Locate every blood parasite and identify its species.
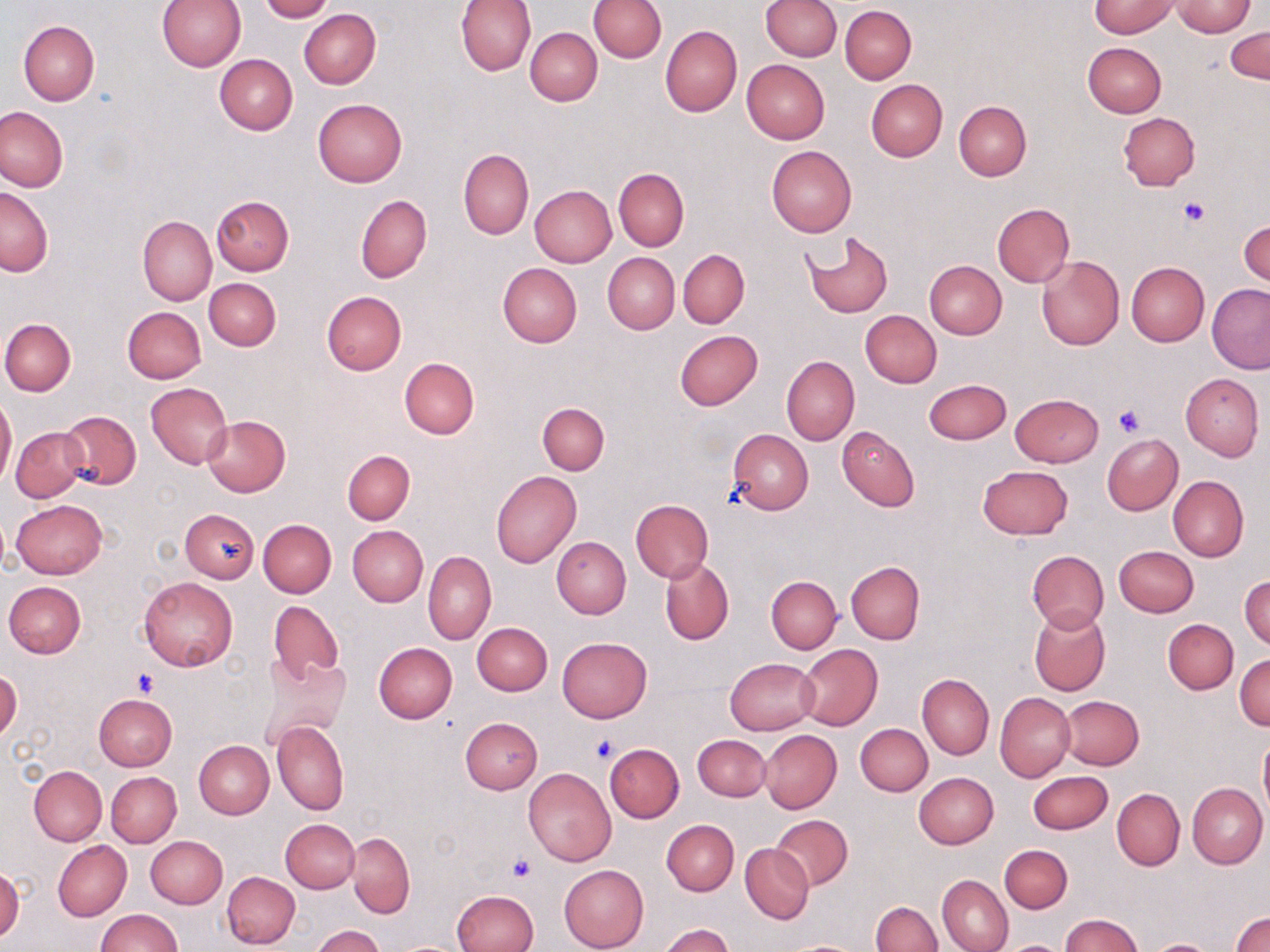
No blood parasites observed.

slide-level diagnosis = negative for blood parasites
uninfected red blood cell locations = approximate bounding boxes as (x1,y1)-(x2,y2) corner pairs in pixels: (259,0)-(332,22), (456,0)-(536,76), (589,0)-(666,63), (761,0)-(841,61), (157,1)-(245,72), (1089,2)-(1180,39), (1171,2)-(1257,37), (840,5)-(917,83), (299,8)-(381,89), (18,20)-(99,104), (660,24)-(742,117), (525,27)-(602,105), (1227,27)-(1270,84), (1083,42)-(1167,117), (215,53)-(297,134), (741,59)-(830,143), (866,80)-(947,161), (312,98)-(407,188), (954,100)-(1031,181), (0,106)-(70,193), (1118,113)-(1200,191), (766,145)-(857,236), (458,149)-(534,239), (614,169)-(689,251), (530,185)-(616,267), (0,187)-(54,276), (211,194)-(294,275), (355,195)-(432,283), (992,203)-(1074,286), (138,215)-(216,306), (1239,220)-(1269,288), (801,230)-(894,319), (679,250)-(749,328), (602,252)-(679,333), (1036,256)-(1124,350), (924,259)-(1007,339), (1126,261)-(1210,346), (498,263)-(582,348), (204,278)-(281,350), (1208,284)-(1270,373), (321,290)-(407,375), (121,306)-(205,383), (861,310)-(941,387), (1,318)-(76,397), (674,331)-(763,410), (782,356)-(859,445), (400,357)-(478,439), (1181,372)-(1264,460), (925,378)-(1011,444), (146,383)-(232,468), (1010,393)-(1104,467), (0,396)-(16,488), (537,402)-(610,475), (58,410)-(141,490), (203,416)-(290,497), (837,426)-(920,512), (11,427)-(87,502), (727,429)-(814,515), (1101,433)-(1183,516), (343,450)-(415,524), (977,465)-(1073,539), (491,470)-(581,568), (1168,476)-(1248,562), (12,500)-(106,578), (631,500)-(713,582), (180,509)-(259,583), (258,519)-(336,598), (346,525)-(428,607), (551,536)-(631,619), (1113,546)-(1198,617), (1027,549)-(1108,632), (424,551)-(496,645), (660,557)-(733,645), (846,561)-(924,644), (1240,574)-(1269,650), (766,575)-(842,653), (138,576)-(237,671), (4,580)-(87,658), (269,601)-(343,683), (1028,608)-(1109,695), (1163,619)-(1238,694), (471,622)-(552,695), (557,636)-(651,722), (374,643)-(457,722), (796,644)-(882,730), (258,653)-(351,745), (1234,653)-(1270,730), (725,657)-(818,735), (0,669)-(22,744), (918,674)-(994,759), (995,691)-(1075,781), (94,693)-(176,772), (1061,695)-(1144,770), (460,717)-(542,794), (273,719)-(349,814), (856,723)-(932,795), (759,730)-(841,813), (694,734)-(770,801), (1258,736)-(1270,821), (194,741)-(273,819), (605,743)-(683,822), (29,766)-(107,845), (523,768)-(617,866), (107,771)-(181,847), (1027,771)-(1114,834), (914,772)-(998,849), (1187,782)-(1267,868), (1112,788)-(1184,870), (771,814)-(852,891), (663,819)-(738,895), (281,820)-(359,893), (346,832)-(414,918), (146,835)-(227,908), (52,840)-(131,922), (741,844)-(814,924), (999,844)-(1073,913), (0,864)-(24,942), (560,865)-(649,952), (222,871)-(299,948), (938,875)-(1014,952), (453,890)-(539,952), (875,890)-(1009,949), (871,901)-(941,952), (95,909)-(181,951), (1232,909)-(1270,952), (1062,914)-(1143,952), (660,924)-(735,952), (312,926)-(385,952), (779,939)-(866,951), (999,940)-(1068,952), (1149,940)-(1216,952)
field of view = one of a larger specimen
preparation = thin blood film
magnification = 1000x
image size = 1270×952 pixels
modality = light microscopy
platelet locations = approximate bounding boxes as (x1,y1)-(x2,y2) corner pairs in pixels: (1178,196)-(1208,227), (1114,406)-(1145,437), (132,670)-(158,697), (591,733)-(621,763), (508,856)-(536,883)
stain = May-Grünwald-Giemsa